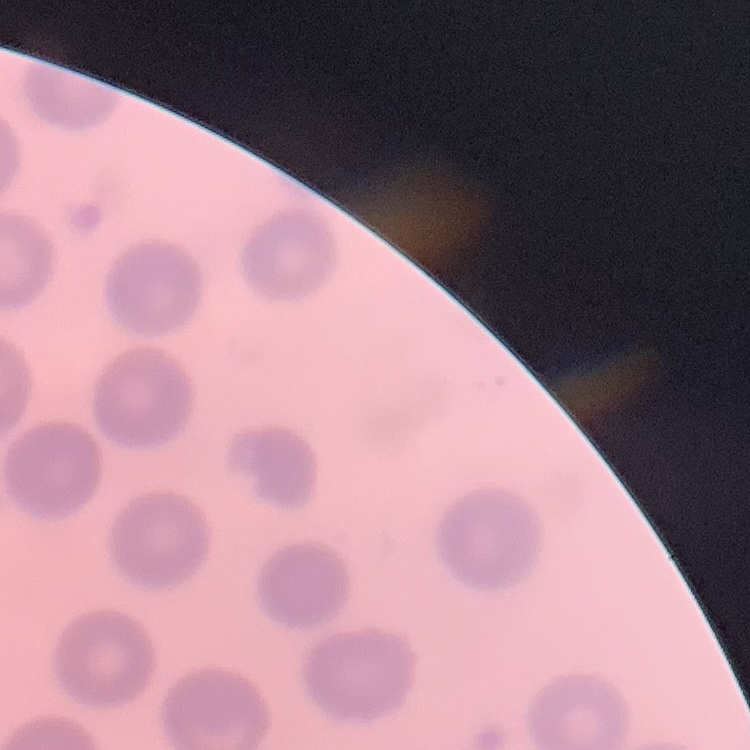

Summary:
  - Erythrocyte morphology: no rouleaux formation
  - Image type: square crop of a larger photomicrograph
  - Stain: Field's or Giemsa
  - Preparation: thin blood smear